Identify the parasite.
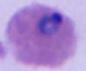
Plasmodium.

magnification = 400x or 1000x
modality = photomicrograph